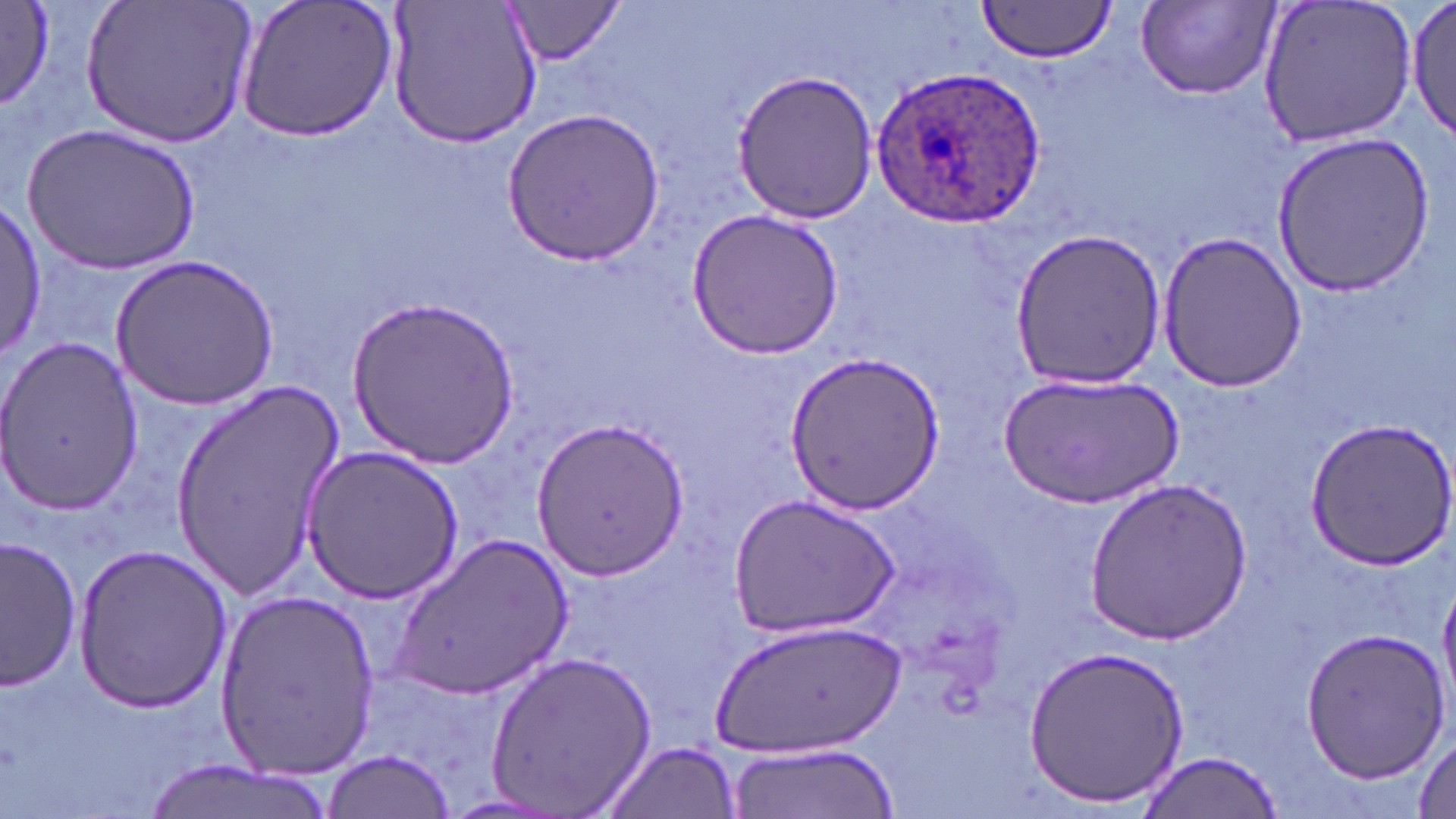

slide-level diagnosis = Plasmodium ovale
magnification = 1000x
Plasmodium ovale-infected red blood cell locations = approximate bounding boxes as named x1/y1/x2/y2 corners in pixels: (x1=871, y1=63, x2=1045, y2=228)
field of view = single
preparation = thin blood smear
stain = May-Grünwald-Giemsa
modality = optical microscopy
image size = 1456×819 pixels
uninfected red blood cell locations = approximate bounding boxes as named x1/y1/x2/y2 corners in pixels: (x1=0, y1=0, x2=63, y2=115), (x1=80, y1=0, x2=254, y2=151), (x1=232, y1=0, x2=402, y2=142), (x1=386, y1=0, x2=543, y2=150), (x1=501, y1=0, x2=628, y2=65), (x1=977, y1=0, x2=1119, y2=63), (x1=1254, y1=0, x2=1421, y2=150), (x1=1408, y1=0, x2=1455, y2=145), (x1=1138, y1=2, x2=1278, y2=100), (x1=734, y1=68, x2=881, y2=224), (x1=502, y1=106, x2=664, y2=265), (x1=25, y1=122, x2=198, y2=275), (x1=1273, y1=131, x2=1437, y2=297), (x1=0, y1=203, x2=44, y2=354), (x1=686, y1=207, x2=844, y2=360), (x1=1005, y1=226, x2=1167, y2=390), (x1=1155, y1=229, x2=1307, y2=392), (x1=111, y1=254, x2=279, y2=409), (x1=346, y1=297, x2=521, y2=466), (x1=0, y1=334, x2=145, y2=518), (x1=783, y1=351, x2=944, y2=517), (x1=1000, y1=370, x2=1184, y2=508), (x1=168, y1=378, x2=346, y2=599), (x1=1300, y1=415, x2=1456, y2=571), (x1=531, y1=419, x2=692, y2=577), (x1=299, y1=443, x2=462, y2=604), (x1=1085, y1=474, x2=1251, y2=647), (x1=729, y1=494, x2=897, y2=637), (x1=391, y1=532, x2=573, y2=701), (x1=2, y1=537, x2=83, y2=689), (x1=73, y1=542, x2=231, y2=714), (x1=215, y1=588, x2=380, y2=777), (x1=716, y1=617, x2=900, y2=755), (x1=1298, y1=628, x2=1448, y2=780), (x1=1024, y1=645, x2=1189, y2=809), (x1=484, y1=649, x2=658, y2=816), (x1=1412, y1=737, x2=1454, y2=818), (x1=724, y1=740, x2=894, y2=817), (x1=598, y1=741, x2=743, y2=819), (x1=321, y1=749, x2=458, y2=816), (x1=1135, y1=749, x2=1285, y2=817), (x1=140, y1=761, x2=337, y2=819)